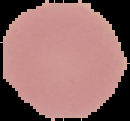

Result: no Plasmodium parasites seen. Image is 130×121 pixels. From a thin blood smear. Segmented cell region on a black background.